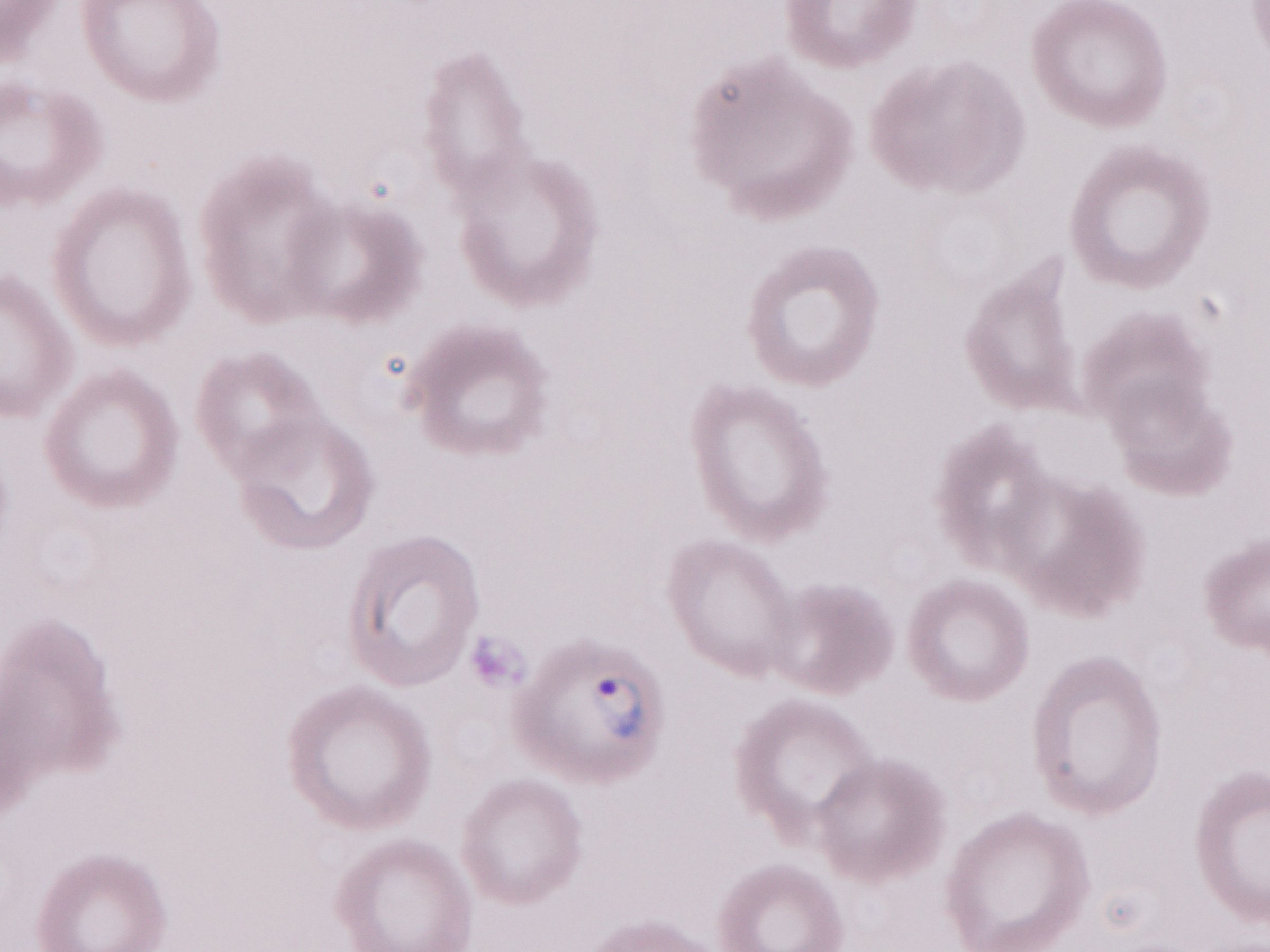 Image is 1270×952 pixels. Single field of view. Thin blood film. Olympus BX43 microscope and DP73 digital camera. Patient diagnosis: malaria infection. May-Grünwald-Giemsa stain. Magnification: 1,000x.